Name the parasite shown.
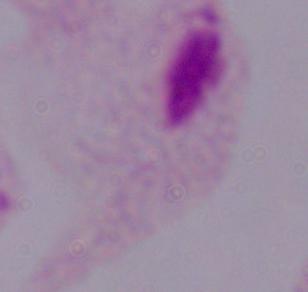
This is a trichomonad.

Summary:
  - Modality: photomicrograph
  - Magnification: 1000x